Locate every blood parasite and identify its species.
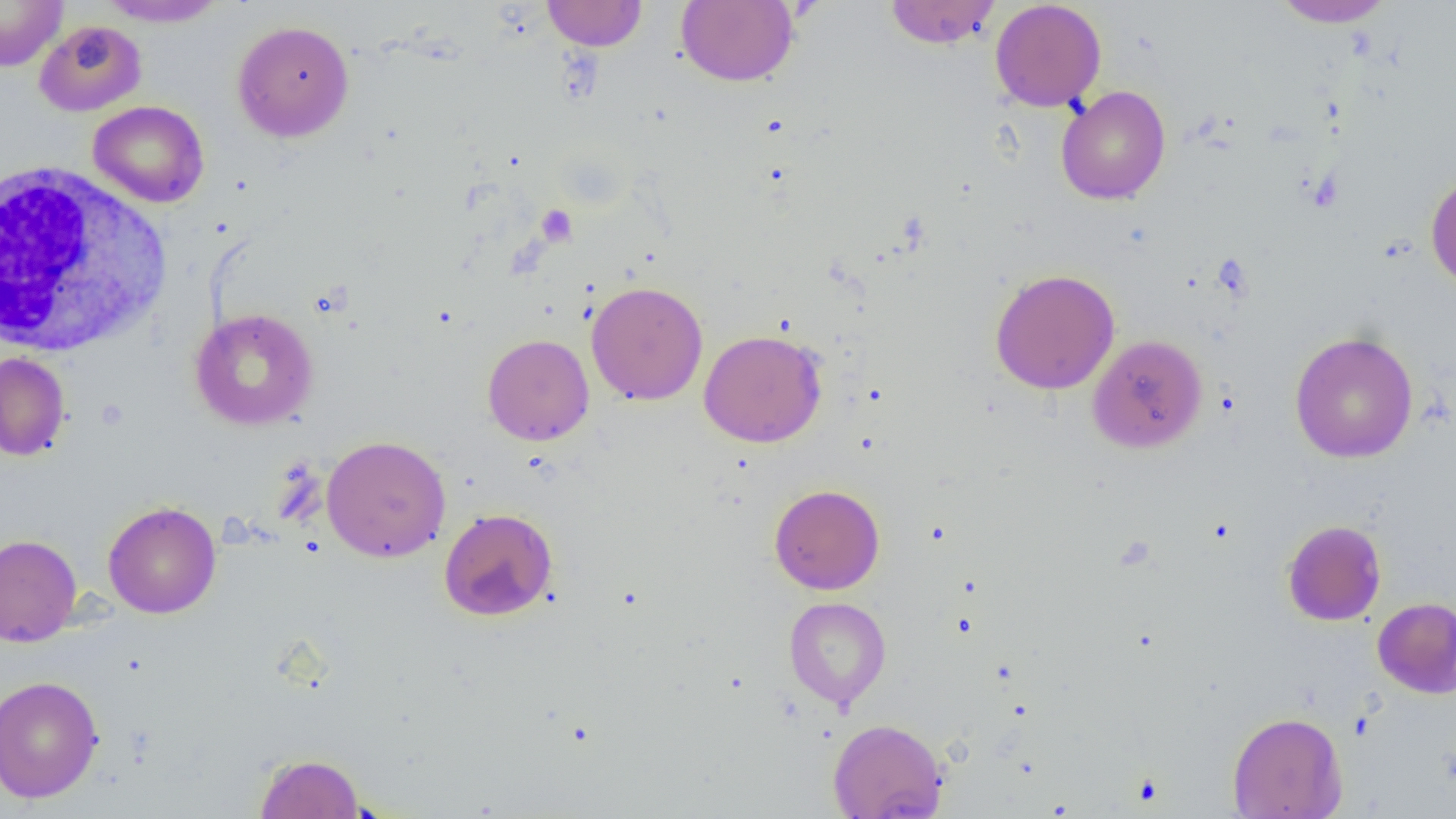
No blood parasites observed.

Summary:
  - Coordinate format: approximate bounding boxes as named x1/y1/x2/y2 corners in pixels
  - Uninfected red blood cell locations: (x1=0, y1=0, x2=68, y2=71), (x1=97, y1=0, x2=228, y2=27), (x1=542, y1=0, x2=647, y2=51), (x1=676, y1=0, x2=798, y2=87), (x1=884, y1=0, x2=1001, y2=49), (x1=989, y1=0, x2=1107, y2=112), (x1=1271, y1=0, x2=1396, y2=28), (x1=34, y1=20, x2=147, y2=117), (x1=232, y1=20, x2=355, y2=143), (x1=1056, y1=85, x2=1171, y2=205), (x1=88, y1=100, x2=209, y2=207), (x1=1425, y1=171, x2=1456, y2=292), (x1=990, y1=268, x2=1120, y2=395), (x1=586, y1=280, x2=708, y2=405), (x1=190, y1=308, x2=318, y2=430), (x1=699, y1=329, x2=826, y2=447), (x1=1289, y1=331, x2=1419, y2=463), (x1=482, y1=334, x2=594, y2=445), (x1=1087, y1=334, x2=1208, y2=453), (x1=0, y1=352, x2=71, y2=461), (x1=321, y1=435, x2=451, y2=563), (x1=769, y1=484, x2=884, y2=595), (x1=102, y1=501, x2=221, y2=618), (x1=439, y1=508, x2=558, y2=621), (x1=1281, y1=520, x2=1387, y2=626), (x1=0, y1=534, x2=82, y2=647), (x1=783, y1=596, x2=891, y2=710), (x1=1373, y1=597, x2=1456, y2=698), (x1=0, y1=675, x2=104, y2=803), (x1=1227, y1=711, x2=1347, y2=818), (x1=827, y1=718, x2=947, y2=819), (x1=254, y1=752, x2=365, y2=818)
  - White blood cell locations: (x1=0, y1=161, x2=173, y2=359)
  - Platelet locations: (x1=536, y1=205, x2=577, y2=246)
  - Slide-level diagnosis: negative for blood parasites
  - Field of view: single
  - Modality: light microscopy
  - Preparation: thin blood smear
  - Magnification: 1000x
  - Image size: 1456×819 pixels